Assess this cell for malaria.
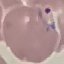
Parasitized.

Cell patch, automatically extracted from a larger field of view and resized to 64 × 64 pixels. Thin blood smear. Photographed with a smartphone camera at the microscope eyepiece. Giemsa-stained preparation.